Report the malaria status of this cell.
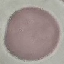

Uninfected.

image type = cell patch, automatically extracted from a larger field of view and resized to 64 × 64 pixels
capture = smartphone camera at the microscope eyepiece
stain = Giemsa
preparation = thin blood film